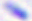

magnification: 400x
modality: photomicrograph
identification: Toxoplasma gondii